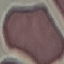
result = no malaria parasites seen
capture = smartphone camera at the microscope eyepiece
preparation = thin blood smear
image type = cell patch, automatically extracted from a larger field of view and resized to 64 × 64 pixels
stain = Giemsa